Comment on the morphology of the red blood cells.
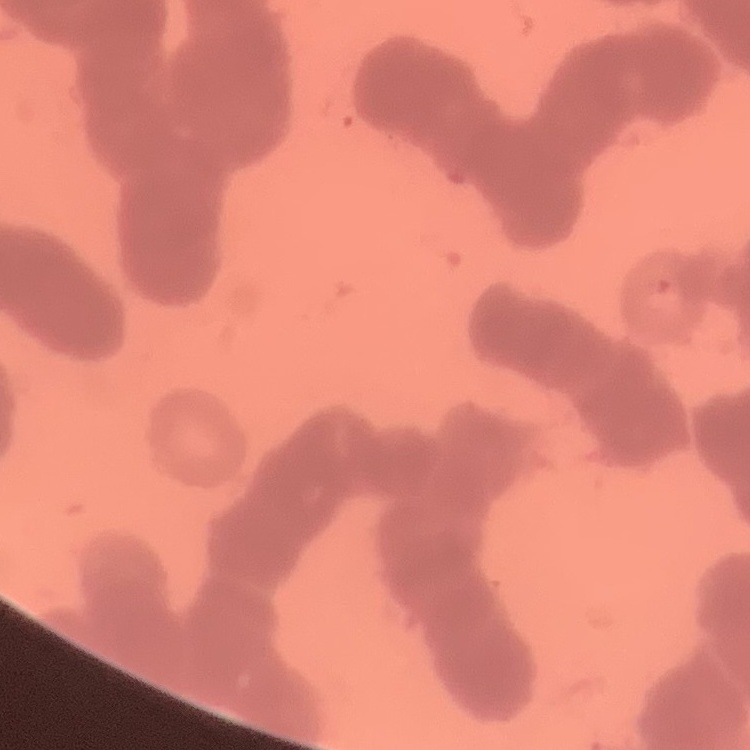
They show rouleaux formation.

Summary:
  - Stain: Field's or Giemsa
  - Image type: one tile cut from a larger photomicrograph
  - Preparation: thin blood film